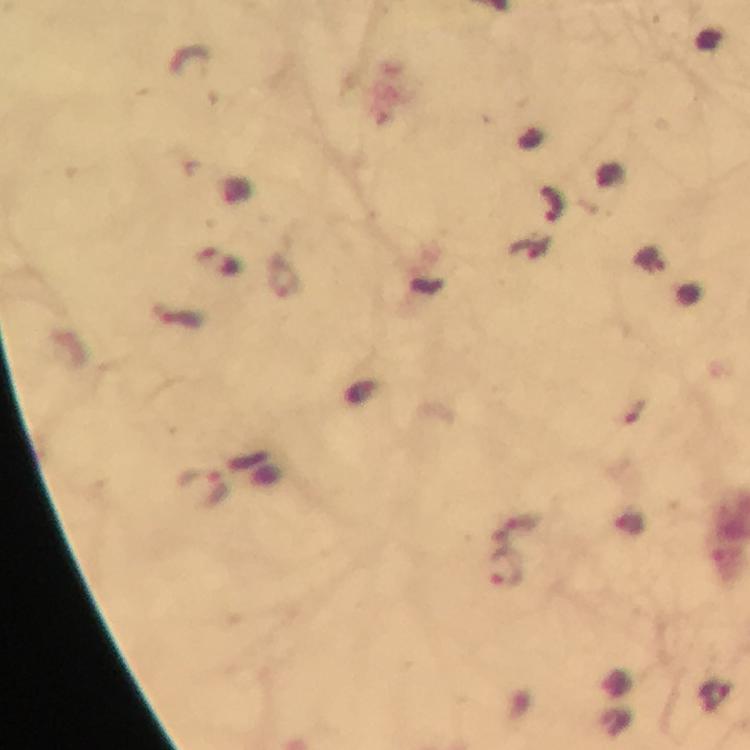
preparation: thick smear
image_size: 750×750 pixels
context: from a diagnostic examination for malaria
stain: Giemsa
immersion_oil: applied
capture: smartphone mounted on the microscope
magnification: 100x
plasmodium_parasite_locations: 'approximate object centers, in pixels from the top-left corner: (x=552, y=203), (x=178, y=317), (x=202, y=488), (x=516, y=528), (x=506, y=568), (x=718, y=697)'
cropped_from: one field of view